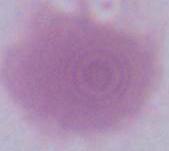
identification = erythrocyte
modality = micrograph
magnification = 1000x